Classify this cell by malaria status.
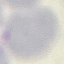
It is uninfected.

preparation = thin smear
image type = cell patch, automatically extracted from a larger field of view and resized to 64 × 64 pixels
stain = Giemsa
capture = smartphone camera at the microscope eyepiece